Name the cell type shown.
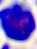
A leukocyte.

Summary:
  - Modality: photomicrograph
  - Magnification: 400x